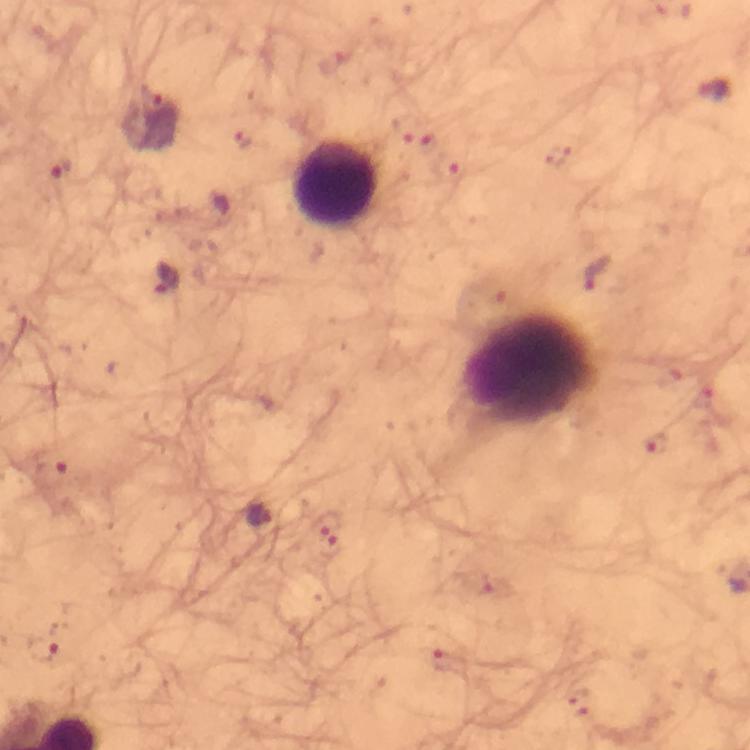
Approximate object centers, in pixels from the top-left corner.
Summary:
  - Leukocyte locations: (x=334, y=184), (x=530, y=369)
  - Malaria parasite locations: (x=156, y=101), (x=599, y=274), (x=165, y=279), (x=655, y=446), (x=259, y=518), (x=330, y=528), (x=38, y=646)
  - Immersion oil: used
  - Image size: 750×750 pixels
  - Magnification: 100x
  - Capture: smartphone mounted on the microscope
  - Preparation: thick blood film
  - Stain: Giemsa
  - Cropped from: one field of view
  - Context: from a diagnostic examination for malaria